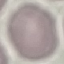
Result: negative for malaria parasites. Giemsa-stained preparation. Automatically extracted cell patch, resized to 64 × 64 pixels. Acquired by smartphone through the microscope eyepiece. Thin blood smear.